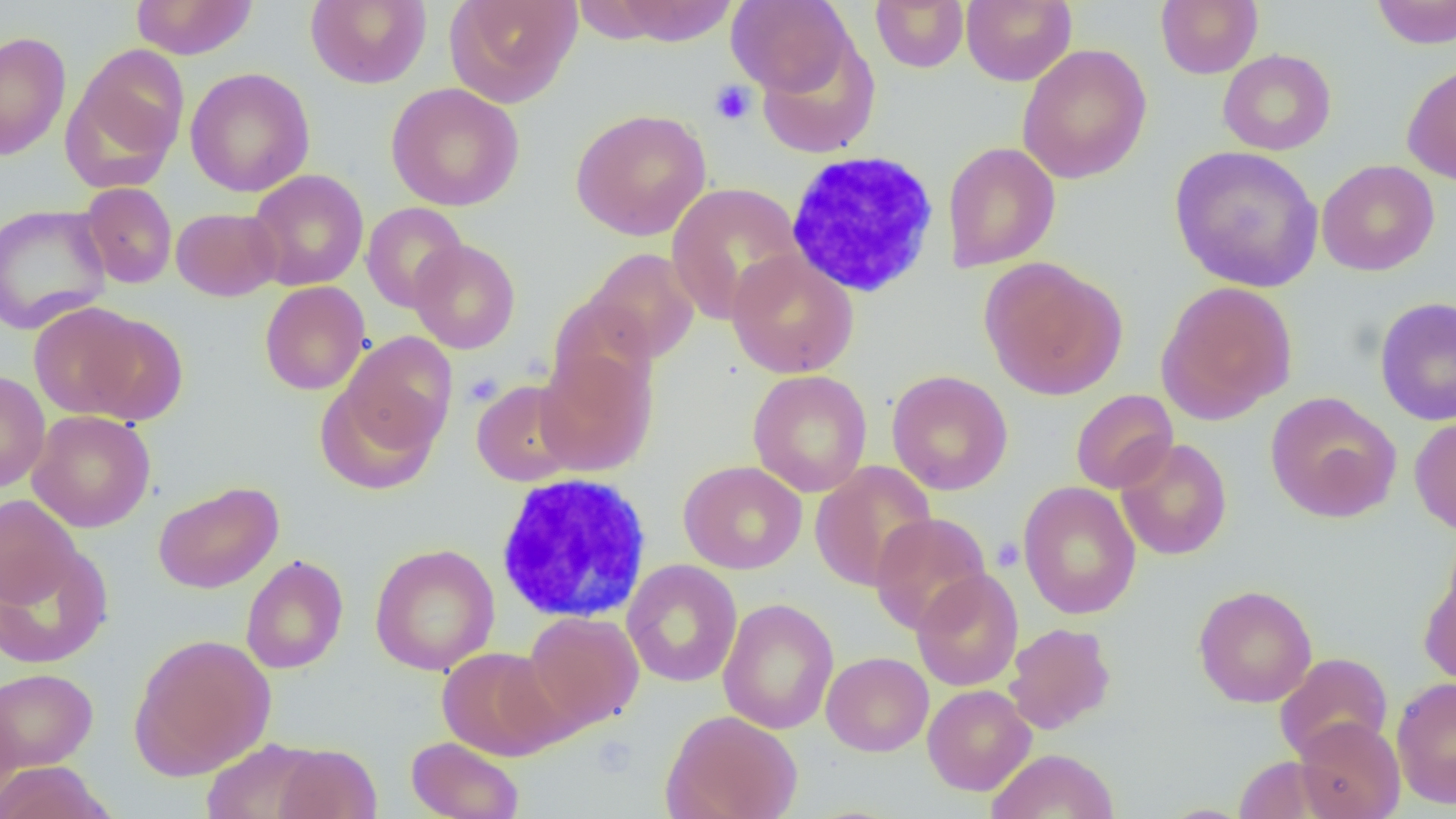 Approximate bounding boxes as named x1/y1/x2/y2 corners in pixels. White blood cell locations: (x1=798, y1=153, x2=937, y2=296), (x1=493, y1=473, x2=653, y2=625). Uninfected red blood cell locations: (x1=130, y1=0, x2=259, y2=60), (x1=305, y1=0, x2=432, y2=89), (x1=444, y1=0, x2=582, y2=108), (x1=870, y1=0, x2=969, y2=72), (x1=961, y1=0, x2=1077, y2=86), (x1=1155, y1=0, x2=1263, y2=78), (x1=1371, y1=0, x2=1456, y2=49), (x1=605, y1=1, x2=739, y2=46), (x1=727, y1=1, x2=854, y2=96), (x1=0, y1=30, x2=71, y2=161), (x1=756, y1=35, x2=881, y2=159), (x1=1017, y1=43, x2=1152, y2=184), (x1=63, y1=44, x2=190, y2=186), (x1=1217, y1=48, x2=1336, y2=155), (x1=1401, y1=62, x2=1456, y2=186), (x1=185, y1=67, x2=315, y2=197), (x1=385, y1=82, x2=525, y2=211), (x1=570, y1=108, x2=711, y2=241), (x1=942, y1=142, x2=1061, y2=272), (x1=1169, y1=146, x2=1324, y2=294), (x1=1316, y1=159, x2=1440, y2=277), (x1=247, y1=168, x2=369, y2=291), (x1=77, y1=181, x2=177, y2=289), (x1=666, y1=182, x2=805, y2=324), (x1=361, y1=202, x2=468, y2=313), (x1=0, y1=204, x2=112, y2=334), (x1=171, y1=207, x2=282, y2=301), (x1=409, y1=239, x2=521, y2=354), (x1=584, y1=248, x2=700, y2=364), (x1=726, y1=249, x2=859, y2=379), (x1=979, y1=257, x2=1128, y2=401), (x1=259, y1=281, x2=371, y2=395), (x1=1156, y1=281, x2=1298, y2=423), (x1=547, y1=294, x2=658, y2=405), (x1=1374, y1=296, x2=1456, y2=427), (x1=29, y1=301, x2=152, y2=421), (x1=79, y1=312, x2=189, y2=423), (x1=339, y1=332, x2=457, y2=456), (x1=534, y1=347, x2=657, y2=476), (x1=747, y1=369, x2=873, y2=497), (x1=0, y1=370, x2=50, y2=492), (x1=887, y1=370, x2=1013, y2=496), (x1=471, y1=379, x2=584, y2=486), (x1=315, y1=381, x2=441, y2=495), (x1=1070, y1=389, x2=1178, y2=494), (x1=1264, y1=391, x2=1402, y2=523), (x1=27, y1=410, x2=156, y2=532), (x1=1409, y1=415, x2=1456, y2=535), (x1=1115, y1=437, x2=1232, y2=561), (x1=679, y1=460, x2=807, y2=574), (x1=810, y1=461, x2=937, y2=591), (x1=153, y1=481, x2=284, y2=594), (x1=1018, y1=481, x2=1141, y2=620), (x1=0, y1=494, x2=81, y2=606), (x1=869, y1=512, x2=991, y2=636), (x1=0, y1=543, x2=113, y2=669), (x1=369, y1=543, x2=500, y2=675), (x1=240, y1=554, x2=348, y2=674), (x1=622, y1=559, x2=742, y2=688), (x1=912, y1=568, x2=1024, y2=692), (x1=1419, y1=568, x2=1456, y2=687), (x1=1193, y1=584, x2=1318, y2=708), (x1=718, y1=598, x2=839, y2=735), (x1=523, y1=610, x2=645, y2=733), (x1=1004, y1=622, x2=1116, y2=734), (x1=129, y1=633, x2=276, y2=779), (x1=437, y1=646, x2=566, y2=760), (x1=821, y1=651, x2=933, y2=757), (x1=1275, y1=652, x2=1393, y2=762), (x1=0, y1=667, x2=99, y2=772), (x1=1391, y1=676, x2=1456, y2=808), (x1=922, y1=684, x2=1036, y2=795), (x1=0, y1=692, x2=22, y2=816), (x1=662, y1=709, x2=803, y2=819), (x1=1293, y1=716, x2=1405, y2=819), (x1=405, y1=736, x2=525, y2=819), (x1=201, y1=738, x2=326, y2=819), (x1=270, y1=743, x2=382, y2=818), (x1=985, y1=748, x2=1120, y2=819), (x1=1232, y1=756, x2=1332, y2=818), (x1=0, y1=761, x2=115, y2=819). Platelet locations: (x1=709, y1=80, x2=756, y2=126), (x1=463, y1=372, x2=503, y2=406), (x1=991, y1=537, x2=1023, y2=571), (x1=591, y1=734, x2=637, y2=778). Slide-level diagnosis: negative for blood parasites. Light microscopy. Thin blood smear. Single field of view. Captured at 1000x magnification. Image is 1456×819 pixels.